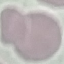 Result: no malaria parasites seen. Cell patch, automatically extracted from a larger field of view and resized to 64 × 64 pixels. Thin smear of blood. Photographed with a smartphone camera at the microscope eyepiece. Giemsa stain.